State the preparation type.
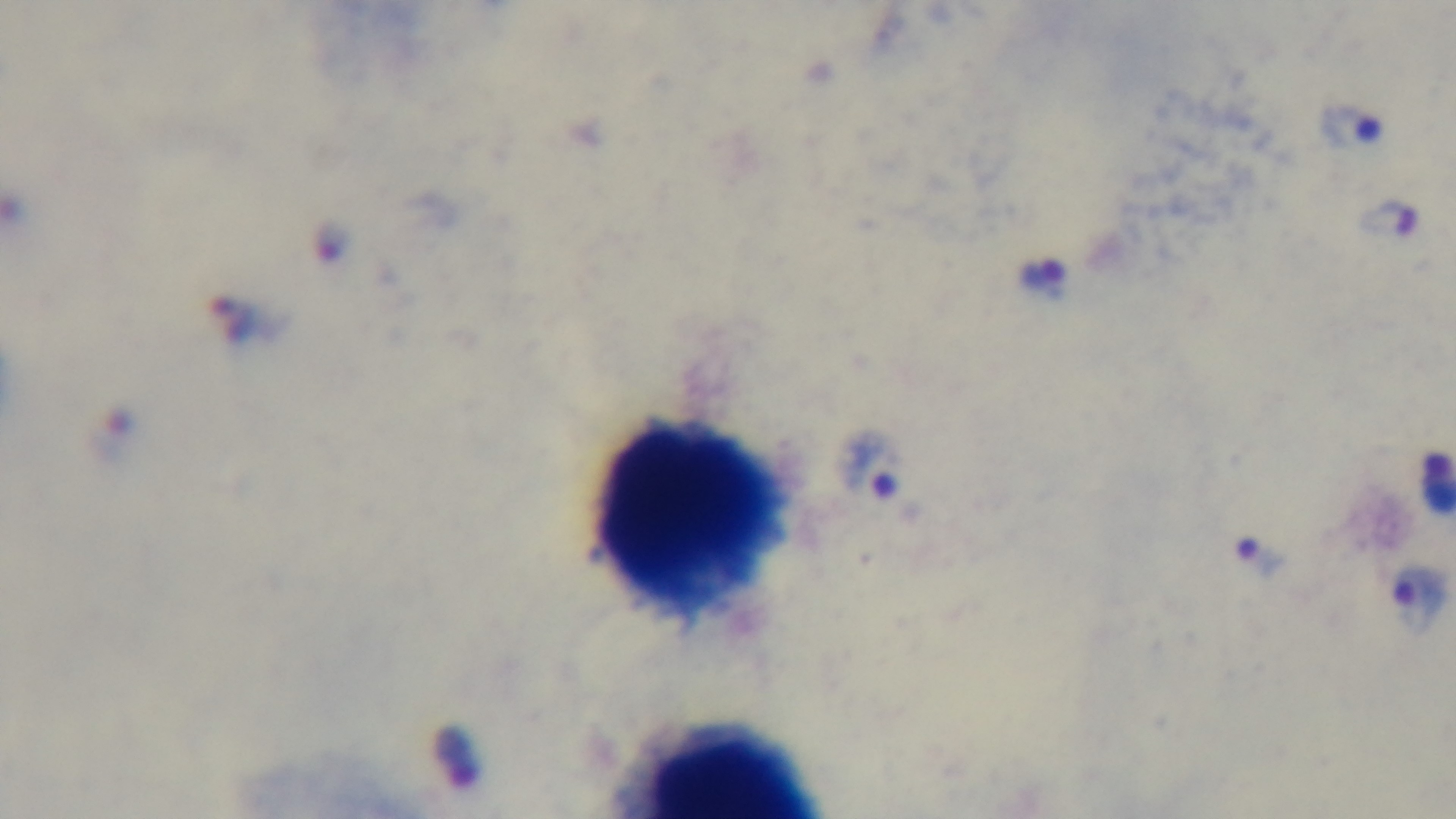

Thick.

{
  "objective": "100x oil immersion",
  "stain": "Giemsa",
  "field_of_view": "single",
  "malaria_status": "infected",
  "modality": "light microscopy",
  "capture": "mounted 4K digital camera"
}